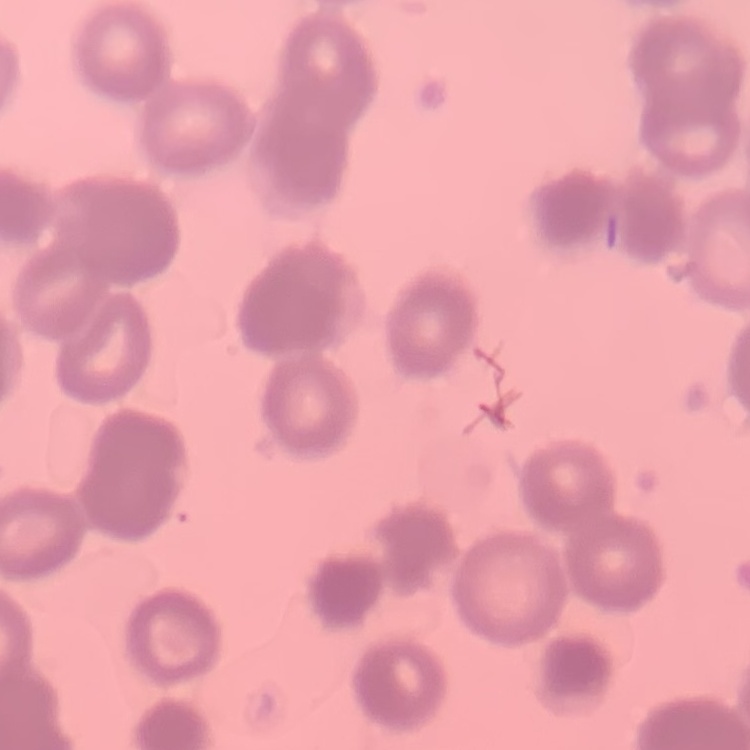
The erythrocytes show rouleaux formation. Stained with either Field's or Giemsa. Thin blood film. Square crop of a larger photomicrograph.